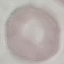

Result: no malaria parasites detected. Thin blood film. Acquired by smartphone through the microscope eyepiece. Cell patch, automatically extracted from a larger field of view and resized to 64 × 64 pixels. Giemsa-stained preparation.